Give the extent of all Plasmodium vivax-infected red blood cells.
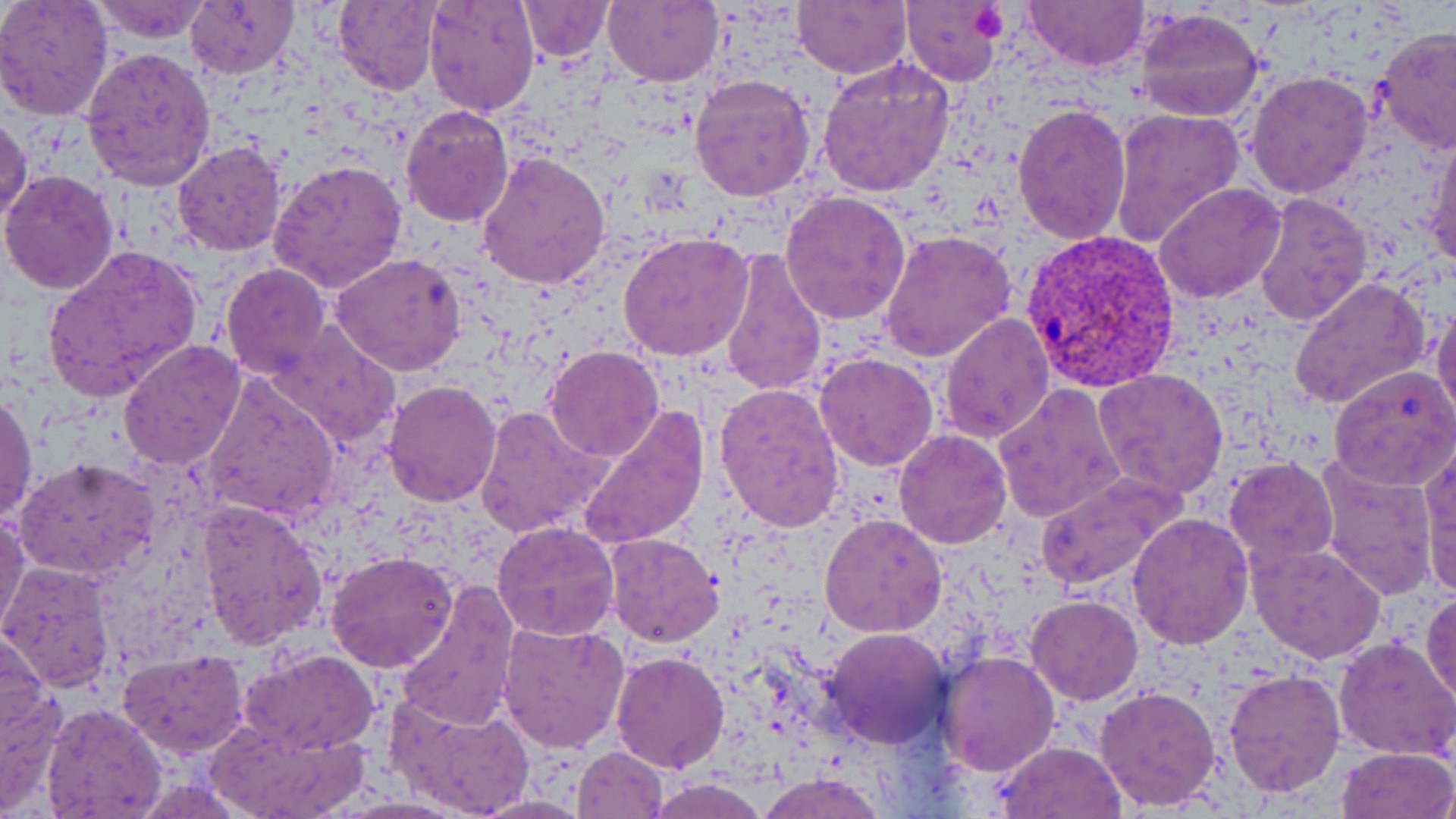

Approximate bounding boxes as [x1, y1, x2, y2] in pixels.
Plasmodium vivax-infected red blood cells: [1020, 229, 1179, 389].

slide-level diagnosis = Plasmodium vivax
platelet locations = approximate bounding boxes as [x1, y1, x2, y2] in pixels: [972, 5, 1010, 43]
uninfected red blood cell locations = approximate bounding boxes as [x1, y1, x2, y2] in pixels: [0, 0, 114, 121], [89, 0, 217, 44], [424, 0, 541, 118], [519, 0, 614, 61], [605, 0, 724, 86], [791, 0, 910, 78], [1021, 0, 1151, 73], [186, 2, 298, 79], [332, 2, 439, 93], [899, 2, 1004, 85], [1133, 7, 1265, 123], [1373, 27, 1456, 154], [82, 46, 216, 191], [818, 59, 957, 197], [1246, 70, 1375, 198], [689, 74, 818, 203], [1012, 103, 1132, 244], [401, 104, 514, 226], [1109, 107, 1245, 248], [0, 113, 32, 226], [1425, 126, 1456, 272], [173, 140, 286, 256], [475, 150, 608, 290], [267, 157, 409, 292], [0, 170, 119, 295], [1155, 180, 1288, 304], [780, 189, 912, 325], [1254, 190, 1373, 326], [880, 228, 1015, 363], [619, 233, 753, 360], [41, 243, 203, 402], [717, 249, 828, 397], [330, 253, 467, 376], [220, 263, 330, 379], [1288, 275, 1432, 412], [1431, 299, 1456, 432], [937, 312, 1054, 444], [268, 322, 402, 447], [118, 340, 246, 471], [544, 346, 665, 462], [815, 353, 939, 472], [1329, 366, 1456, 492], [1093, 368, 1229, 500], [199, 371, 342, 523], [384, 380, 502, 506], [714, 382, 846, 531], [993, 384, 1127, 524], [0, 389, 36, 526], [476, 404, 608, 539], [576, 407, 709, 550], [894, 428, 1011, 548], [1420, 446, 1455, 596], [1225, 456, 1340, 569], [1314, 457, 1437, 599], [15, 458, 158, 581], [1034, 471, 1187, 590], [198, 498, 327, 651], [0, 509, 28, 640], [1127, 513, 1253, 649], [819, 514, 947, 637], [492, 520, 620, 641], [604, 532, 725, 646], [1247, 540, 1385, 663], [325, 551, 458, 673], [2, 563, 116, 692], [398, 582, 519, 730], [1422, 590, 1456, 711], [1026, 596, 1144, 705], [498, 619, 629, 756], [0, 624, 53, 757], [823, 627, 951, 748], [1333, 634, 1456, 761], [242, 647, 379, 755], [119, 649, 249, 758], [609, 650, 729, 773], [936, 651, 1058, 775], [1223, 669, 1346, 796], [0, 680, 68, 817], [1094, 684, 1221, 812], [385, 692, 535, 819], [40, 703, 166, 819], [205, 716, 372, 817], [994, 740, 1129, 818], [572, 745, 668, 819], [1335, 746, 1455, 818], [756, 772, 887, 818], [648, 777, 770, 819], [470, 792, 592, 818], [332, 796, 472, 818]
magnification = 1000x
image size = 1456×819 pixels
modality = optical microscopy
stain = May-Grünwald-Giemsa
field of view = one of a larger specimen
preparation = thin blood film